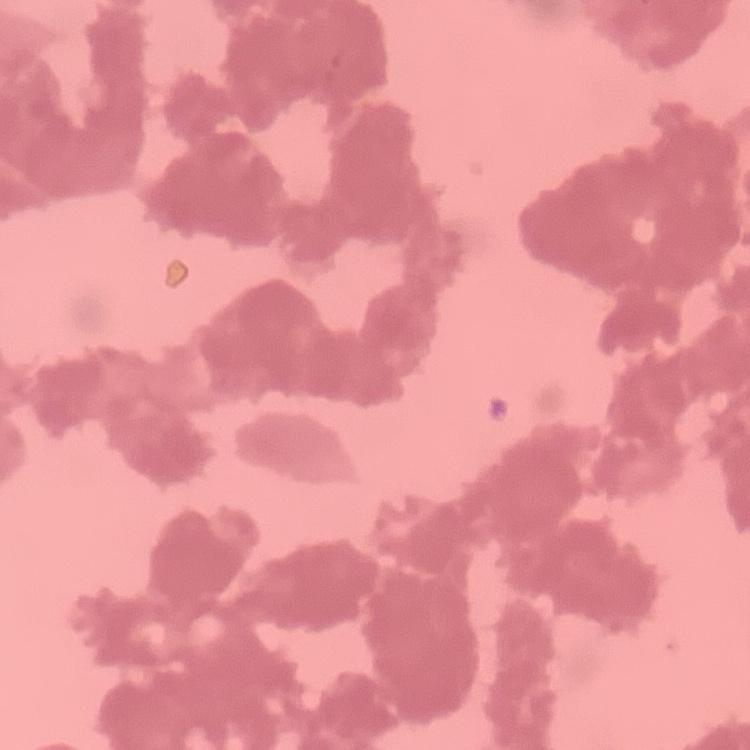

erythrocyte morphology = rouleaux formation
stain = Field's or Giemsa
preparation = thin blood film
image type = one tile cut from a larger photomicrograph